State which parasite is depicted.
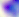
This is Toxoplasma gondii.

modality = photomicrograph
magnification = 400x